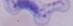

magnification = 1000x
modality = micrograph
identification = trypanosome